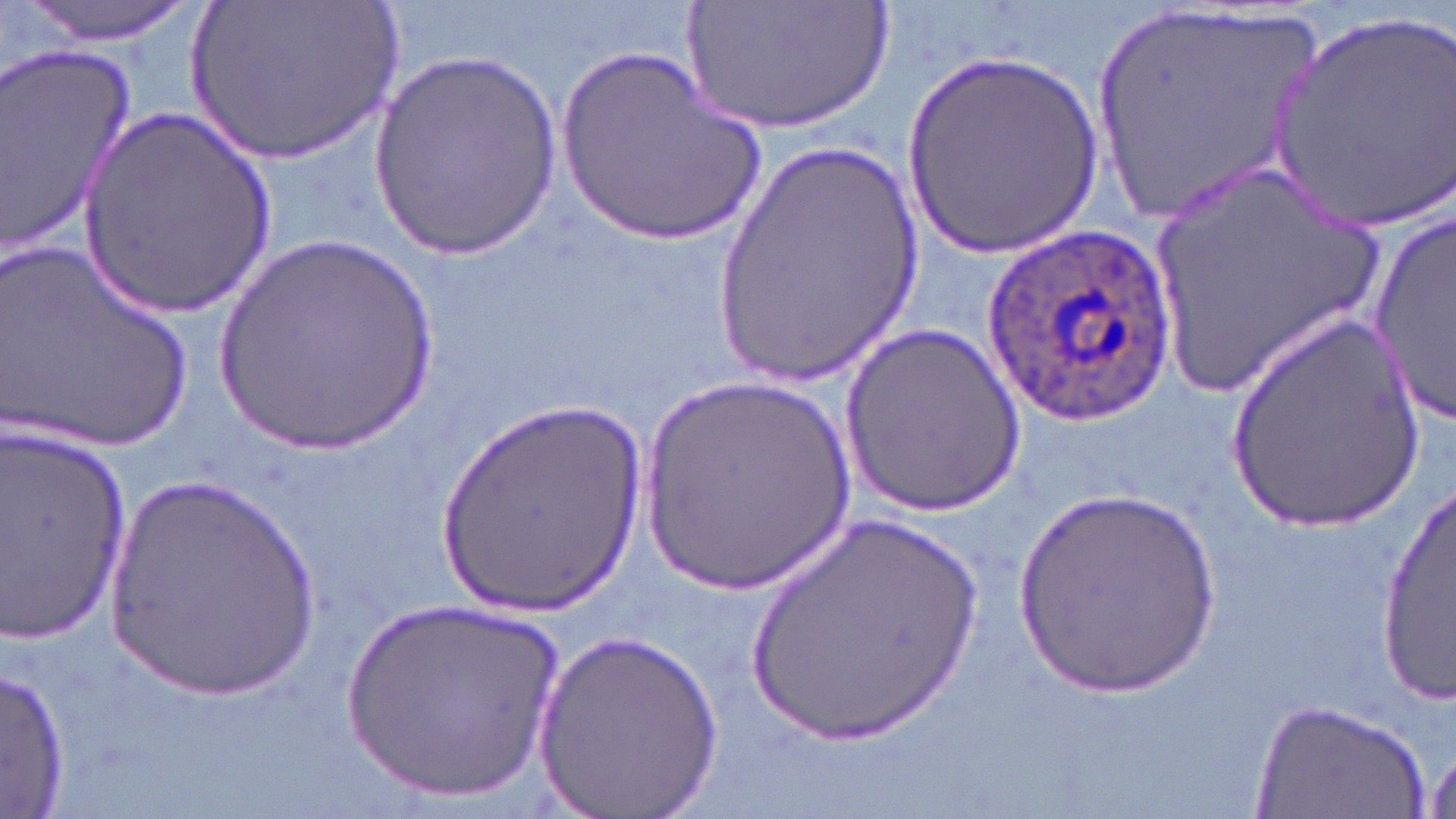
{
  "slide_level_diagnosis": "Plasmodium ovale",
  "stain": "May-Grünwald-Giemsa",
  "magnification": "1000x",
  "plasmodium_ovale_infected_red_blood_cell_locations": "approximate bounding boxes as (x1,y1)-(x2,y2) corner pairs in pixels: (983,224)-(1178,425)",
  "preparation": "thin blood smear",
  "image_size": "1456×819 pixels",
  "field_of_view": "single",
  "modality": "light microscopy",
  "uninfected_red_blood_cell_locations": "approximate bounding boxes as (x1,y1)-(x2,y2) corner pairs in pixels: (15,0)-(201,47), (179,0)-(405,170), (682,0)-(897,140), (1094,7)-(1323,226), (1264,8)-(1455,231), (554,43)-(769,251), (0,45)-(137,255), (370,50)-(562,261), (902,53)-(1102,261), (76,105)-(277,319), (708,136)-(928,385), (1141,158)-(1388,408), (1367,204)-(1455,431), (213,235)-(444,457), (1,241)-(194,454), (1218,307)-(1432,538), (843,323)-(1024,518), (637,376)-(857,598), (430,396)-(648,624), (3,422)-(131,646), (1372,464)-(1454,712), (94,469)-(323,702), (1009,488)-(1221,699), (738,506)-(994,753), (335,591)-(572,802), (535,624)-(725,819), (3,663)-(72,811), (1249,695)-(1434,819)"
}